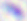

Summary:
  - Modality: photomicrograph
  - Identification: Toxoplasma gondii
  - Magnification: 400x